Assess this cell for malaria.
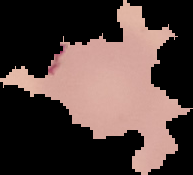

It is uninfected.

{
  "preparation": "thin blood film",
  "image_size": "193×175 pixels",
  "image_type": "segmented cell region on a black background"
}